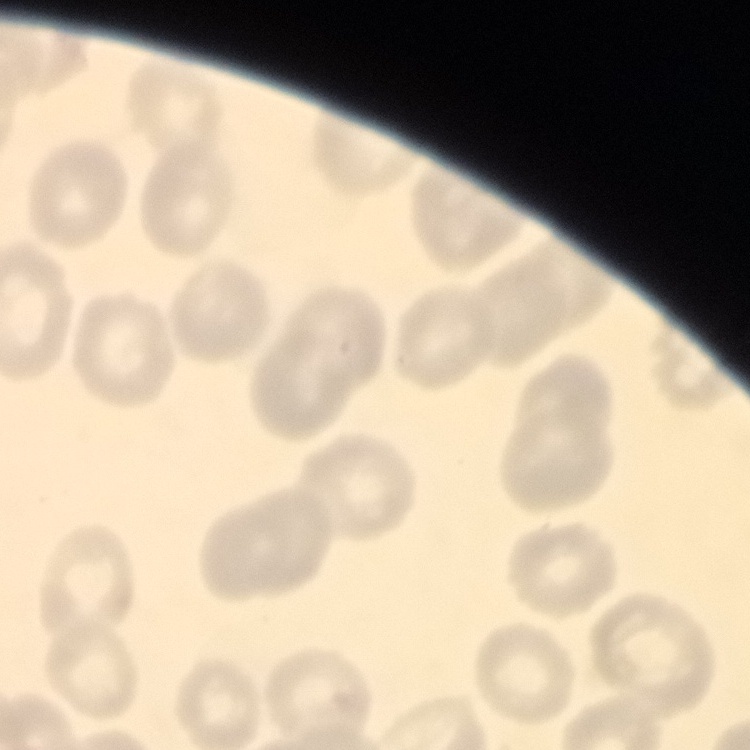

{
  "erythrocyte_morphology": "no rouleaux formation",
  "stain": "Field's or Giemsa",
  "image_type": "one tile cut from a larger photomicrograph",
  "preparation": "thin blood film"
}